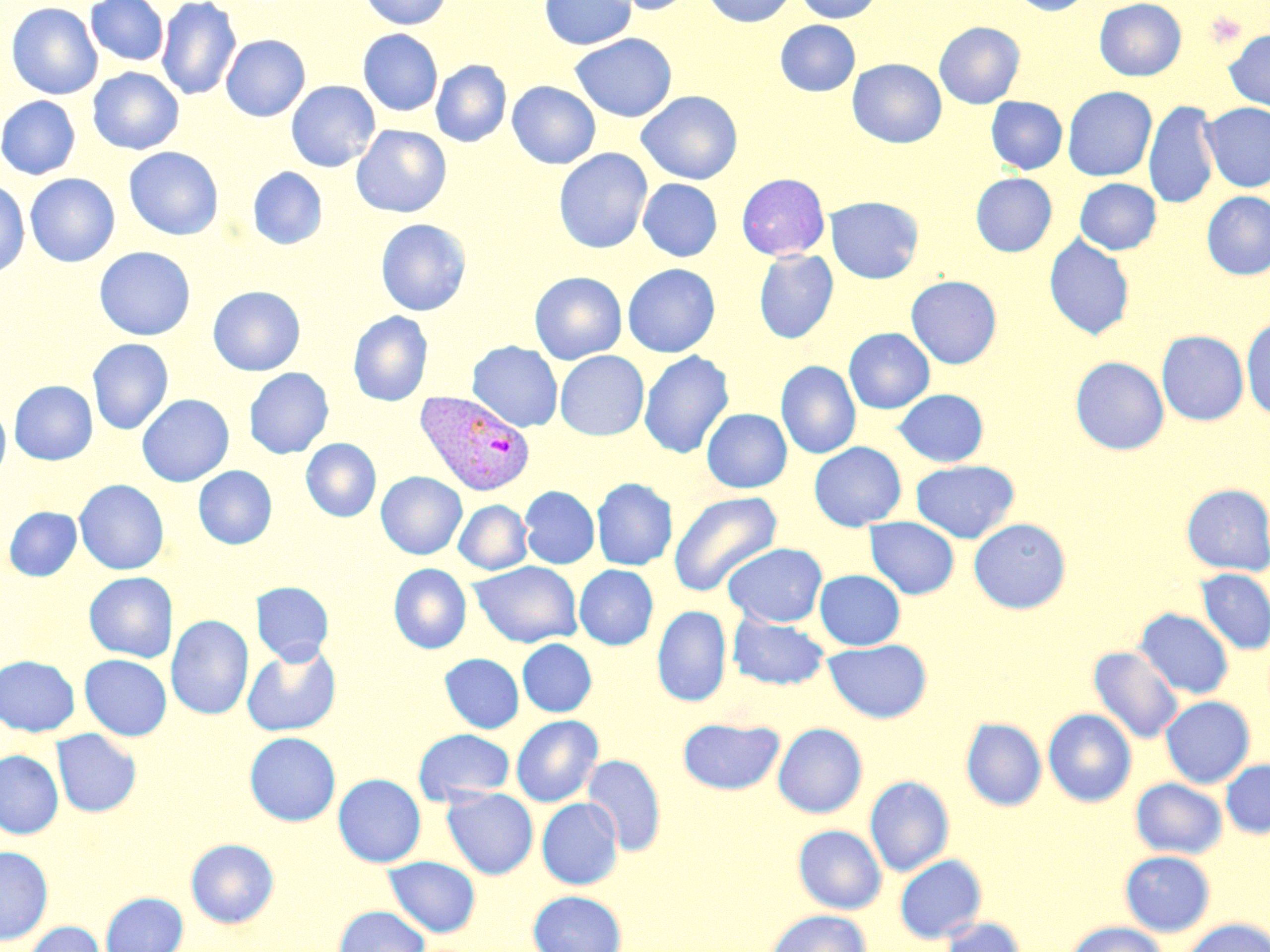

Approximate bounding boxes as named x1/y1/x2/y2 corners in pixels. Platelet locations: (x1=1205, y1=9, x2=1246, y2=47). Plasmodium vivax-infected red blood cell locations: (x1=414, y1=389, x2=536, y2=496). Uninfected red blood cell locations: (x1=86, y1=0, x2=169, y2=67), (x1=156, y1=0, x2=241, y2=101), (x1=359, y1=0, x2=452, y2=29), (x1=539, y1=0, x2=637, y2=50), (x1=608, y1=0, x2=699, y2=15), (x1=704, y1=0, x2=797, y2=27), (x1=794, y1=0, x2=883, y2=23), (x1=1009, y1=0, x2=1094, y2=16), (x1=1094, y1=0, x2=1186, y2=81), (x1=6, y1=2, x2=103, y2=99), (x1=775, y1=20, x2=860, y2=96), (x1=934, y1=21, x2=1025, y2=108), (x1=358, y1=29, x2=443, y2=116), (x1=1223, y1=29, x2=1270, y2=112), (x1=570, y1=33, x2=677, y2=122), (x1=221, y1=34, x2=310, y2=122), (x1=847, y1=58, x2=947, y2=148), (x1=431, y1=60, x2=511, y2=147), (x1=88, y1=67, x2=184, y2=155), (x1=285, y1=80, x2=380, y2=172), (x1=507, y1=81, x2=600, y2=169), (x1=1062, y1=86, x2=1156, y2=181), (x1=637, y1=91, x2=743, y2=184), (x1=0, y1=95, x2=81, y2=179), (x1=986, y1=96, x2=1067, y2=174), (x1=1144, y1=100, x2=1219, y2=210), (x1=1201, y1=102, x2=1270, y2=192), (x1=352, y1=125, x2=451, y2=217), (x1=123, y1=147, x2=223, y2=240), (x1=553, y1=148, x2=653, y2=254), (x1=247, y1=167, x2=327, y2=250), (x1=25, y1=173, x2=120, y2=267), (x1=736, y1=173, x2=830, y2=260), (x1=971, y1=173, x2=1057, y2=256), (x1=638, y1=178, x2=722, y2=262), (x1=1075, y1=178, x2=1161, y2=254), (x1=0, y1=180, x2=29, y2=277), (x1=1201, y1=191, x2=1270, y2=280), (x1=825, y1=196, x2=924, y2=284), (x1=375, y1=219, x2=471, y2=315), (x1=1044, y1=234, x2=1135, y2=340), (x1=94, y1=246, x2=196, y2=340), (x1=754, y1=250, x2=839, y2=343), (x1=622, y1=263, x2=720, y2=357), (x1=530, y1=271, x2=627, y2=364), (x1=546, y1=271, x2=636, y2=440), (x1=906, y1=275, x2=1002, y2=368), (x1=208, y1=285, x2=305, y2=376), (x1=348, y1=311, x2=433, y2=406), (x1=1241, y1=315, x2=1270, y2=420), (x1=844, y1=327, x2=935, y2=413), (x1=1157, y1=330, x2=1248, y2=425), (x1=87, y1=338, x2=173, y2=434), (x1=467, y1=341, x2=563, y2=432), (x1=555, y1=350, x2=649, y2=440), (x1=639, y1=350, x2=734, y2=459), (x1=1070, y1=356, x2=1169, y2=454), (x1=776, y1=360, x2=860, y2=459), (x1=244, y1=367, x2=333, y2=458), (x1=9, y1=380, x2=98, y2=465), (x1=893, y1=389, x2=988, y2=466), (x1=137, y1=394, x2=234, y2=486), (x1=0, y1=403, x2=10, y2=481), (x1=702, y1=408, x2=791, y2=493), (x1=301, y1=438, x2=381, y2=522), (x1=808, y1=442, x2=906, y2=530), (x1=911, y1=460, x2=1019, y2=543), (x1=194, y1=466, x2=277, y2=549), (x1=376, y1=472, x2=467, y2=559), (x1=591, y1=477, x2=677, y2=570), (x1=74, y1=479, x2=169, y2=574), (x1=1182, y1=484, x2=1270, y2=575), (x1=520, y1=486, x2=600, y2=569), (x1=668, y1=490, x2=781, y2=597), (x1=454, y1=500, x2=532, y2=574), (x1=4, y1=507, x2=82, y2=581), (x1=865, y1=517, x2=959, y2=599), (x1=969, y1=518, x2=1071, y2=613), (x1=722, y1=543, x2=828, y2=627), (x1=469, y1=561, x2=583, y2=648), (x1=389, y1=564, x2=471, y2=654), (x1=574, y1=564, x2=659, y2=650), (x1=1196, y1=568, x2=1270, y2=655), (x1=814, y1=569, x2=905, y2=650), (x1=83, y1=571, x2=175, y2=662), (x1=251, y1=581, x2=334, y2=664), (x1=652, y1=605, x2=731, y2=706), (x1=1135, y1=608, x2=1234, y2=699), (x1=727, y1=613, x2=830, y2=690), (x1=167, y1=615, x2=253, y2=720), (x1=823, y1=638, x2=932, y2=723), (x1=517, y1=639, x2=597, y2=717), (x1=242, y1=642, x2=342, y2=736), (x1=1088, y1=645, x2=1183, y2=745), (x1=440, y1=653, x2=524, y2=734), (x1=80, y1=654, x2=172, y2=740), (x1=0, y1=655, x2=80, y2=736), (x1=1160, y1=696, x2=1255, y2=787), (x1=1043, y1=708, x2=1137, y2=807), (x1=511, y1=715, x2=603, y2=806), (x1=678, y1=718, x2=784, y2=794), (x1=961, y1=718, x2=1047, y2=811), (x1=773, y1=723, x2=867, y2=817), (x1=413, y1=728, x2=515, y2=806), (x1=51, y1=729, x2=142, y2=817), (x1=244, y1=731, x2=341, y2=826), (x1=0, y1=749, x2=64, y2=838), (x1=583, y1=754, x2=666, y2=856), (x1=1221, y1=759, x2=1270, y2=837), (x1=333, y1=773, x2=426, y2=867), (x1=865, y1=775, x2=954, y2=876), (x1=1131, y1=777, x2=1227, y2=859), (x1=441, y1=787, x2=538, y2=879), (x1=537, y1=797, x2=623, y2=889), (x1=792, y1=824, x2=887, y2=914), (x1=185, y1=838, x2=279, y2=928), (x1=0, y1=845, x2=53, y2=945), (x1=1120, y1=850, x2=1215, y2=936), (x1=894, y1=854, x2=987, y2=943), (x1=383, y1=856, x2=481, y2=937), (x1=528, y1=890, x2=627, y2=952), (x1=101, y1=891, x2=188, y2=952), (x1=333, y1=905, x2=430, y2=952), (x1=766, y1=909, x2=872, y2=952), (x1=937, y1=916, x2=1027, y2=952), (x1=1180, y1=918, x2=1270, y2=952), (x1=23, y1=921, x2=105, y2=952), (x1=1065, y1=921, x2=1169, y2=952). Slide-level diagnosis: Plasmodium vivax. Thin blood smear. Captured at 1000x magnification. May-Grünwald-Giemsa stain. Optical microscopy. Single field of view. Image is 1270×952 pixels.